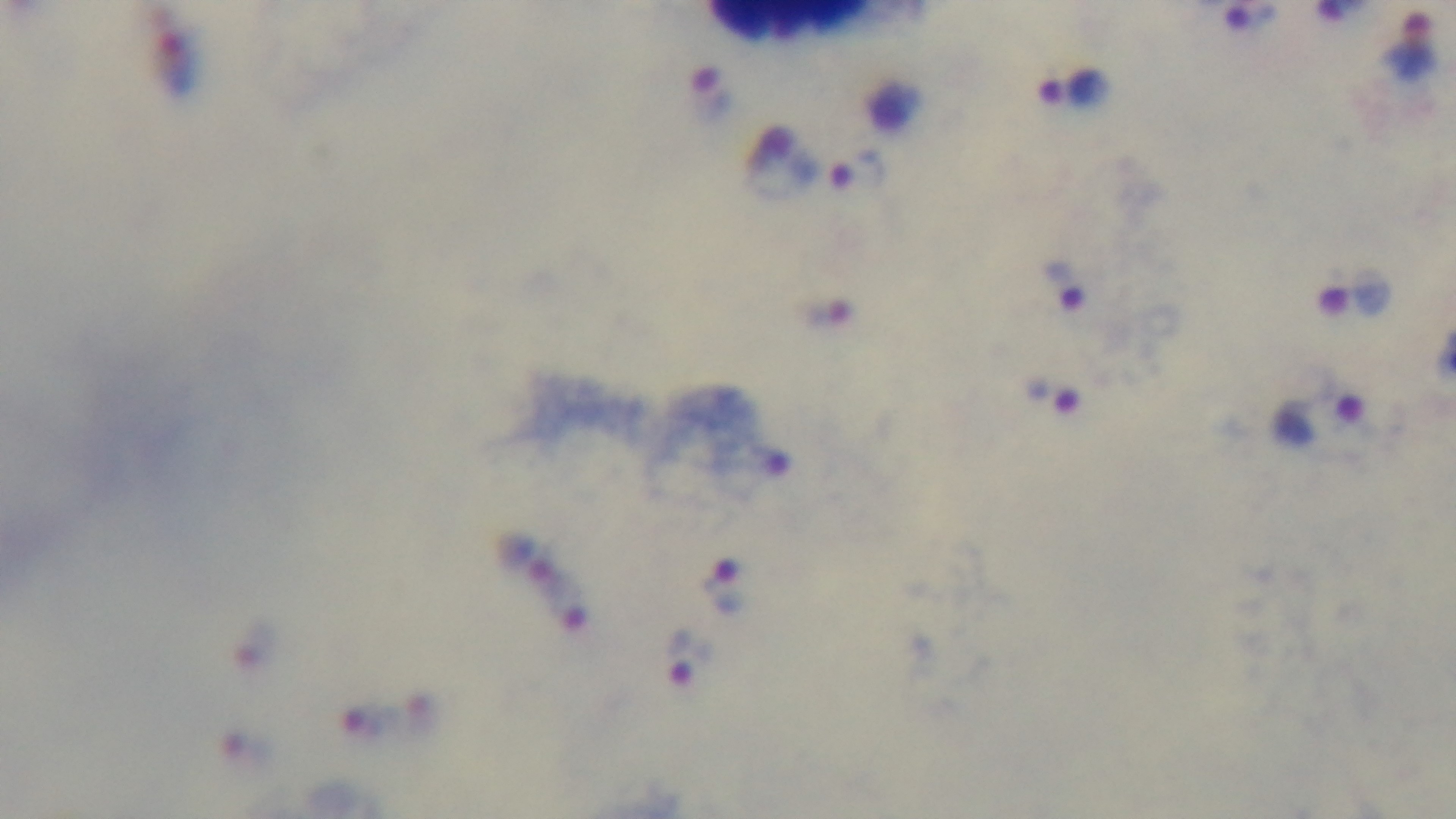

Summary:
  - Stain: Giemsa
  - Malaria status: positive
  - Field of view: one from the slide
  - Capture: mounted 4K digital camera
  - Objective: 100x oil immersion
  - Modality: light microscopy
  - Preparation: thick smear